Outline platelets.
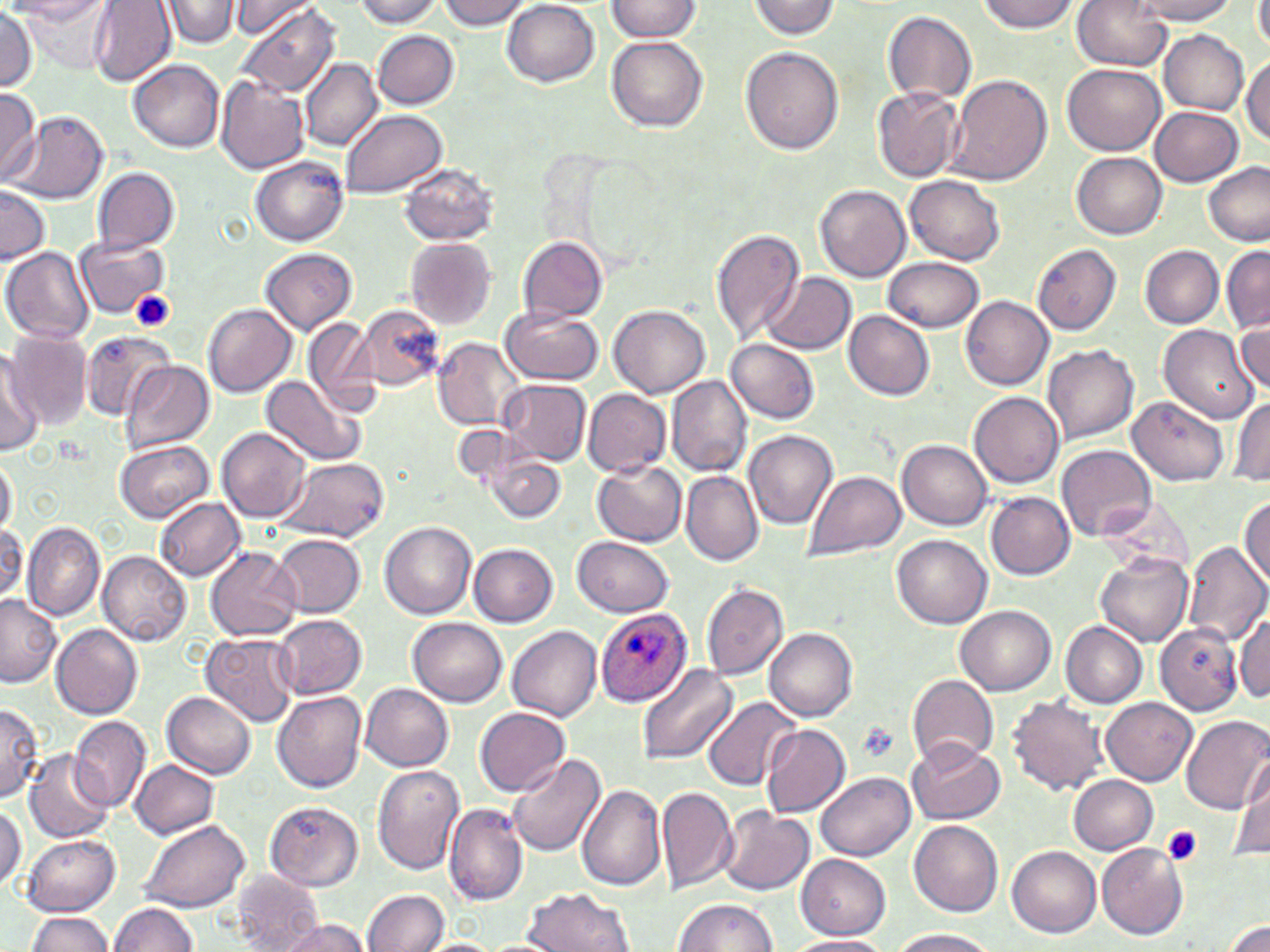

Approximate bounding boxes as (x1,y1)-(x2,y2) corner pairs in pixels.
Platelets: (130,290)-(176,333), (855,721)-(899,762), (1161,826)-(1203,867).

{
  "slide_level_diagnosis": "Plasmodium ovale",
  "modality": "light microscopy",
  "stain": "May-Grünwald-Giemsa",
  "preparation": "thin blood film",
  "image_size": "1270×952 pixels",
  "plasmodium_ovale_infected_red_blood_cell_locations": "approximate bounding boxes as (x1,y1)-(x2,y2) corner pairs in pixels: (597,607)-(692,707)",
  "field_of_view": "single",
  "uninfected_red_blood_cell_locations": "approximate bounding boxes as (x1,y1)-(x2,y2) corner pairs in pixels: (4,0)-(109,23), (21,0)-(120,72), (90,0)-(177,88), (162,0)-(239,47), (353,0)-(444,27), (436,0)-(531,31), (976,0)-(1080,33), (1129,0)-(1240,24), (225,1)-(323,41), (502,1)-(598,86), (604,1)-(703,42), (747,1)-(841,38), (1070,1)-(1174,70), (1252,1)-(1270,51), (238,3)-(342,99), (0,9)-(39,93), (883,11)-(977,104), (1158,29)-(1249,115), (373,30)-(459,110), (608,36)-(708,132), (741,46)-(844,154), (1242,54)-(1270,147), (300,59)-(382,153), (130,60)-(225,152), (1063,64)-(1166,155), (215,75)-(310,173), (947,75)-(1053,187), (872,87)-(964,183), (0,89)-(42,184), (1151,106)-(1243,186), (341,109)-(446,198), (9,111)-(110,204), (1071,152)-(1166,239), (250,155)-(348,247), (1201,160)-(1270,246), (398,163)-(497,247), (92,167)-(179,257), (905,175)-(1006,265), (815,185)-(912,282), (0,186)-(49,266), (710,228)-(804,344), (518,236)-(608,323), (75,237)-(166,318), (404,237)-(497,330), (1033,244)-(1121,336), (1140,245)-(1224,327), (3,247)-(96,343), (1222,247)-(1270,331), (261,248)-(357,334), (884,256)-(983,332), (764,272)-(857,356), (961,296)-(1054,390), (203,303)-(297,397), (357,306)-(444,391), (609,306)-(710,398), (500,308)-(603,385), (844,311)-(935,401), (1233,318)-(1269,397), (304,319)-(380,413), (1157,325)-(1258,424), (79,328)-(175,421), (3,331)-(91,432), (431,337)-(525,432), (726,339)-(819,424), (1042,345)-(1139,445), (0,351)-(41,451), (120,362)-(214,452), (261,375)-(364,466), (667,375)-(751,477), (499,378)-(591,466), (584,388)-(672,478), (968,391)-(1064,487), (1125,396)-(1228,486), (1230,396)-(1270,486), (218,426)-(311,521), (744,429)-(838,530), (898,439)-(993,529), (114,441)-(214,523), (1057,444)-(1157,542), (0,453)-(16,539), (487,453)-(566,523), (277,457)-(387,544), (592,460)-(687,547), (682,471)-(762,565), (804,472)-(905,558), (987,492)-(1074,579), (154,497)-(245,580), (1239,497)-(1270,588), (21,521)-(106,621), (0,522)-(27,607), (379,522)-(477,620), (893,534)-(991,626), (272,535)-(366,617), (573,537)-(674,617), (468,541)-(558,626), (1182,541)-(1269,646), (205,548)-(301,642), (98,550)-(192,646), (1094,552)-(1194,647), (701,582)-(788,681), (0,594)-(64,687), (957,605)-(1057,694), (1234,610)-(1269,703), (275,615)-(367,699), (408,617)-(507,707), (1061,622)-(1147,707), (1154,623)-(1242,714), (51,625)-(144,719), (507,626)-(603,721), (766,628)-(859,721), (203,633)-(299,726), (638,665)-(738,768), (907,673)-(998,770), (361,682)-(453,770), (164,690)-(257,779), (274,691)-(368,792), (1007,694)-(1108,796), (704,696)-(802,792), (1102,696)-(1197,786), (0,703)-(42,802), (475,707)-(570,796), (1180,714)-(1270,814), (69,715)-(150,814), (763,723)-(849,818), (907,738)-(1004,825), (23,749)-(114,844), (509,754)-(606,855), (1242,754)-(1269,831), (131,760)-(217,837), (371,764)-(465,875), (1230,770)-(1270,862), (817,772)-(914,861), (1070,775)-(1158,855), (577,784)-(666,892), (656,784)-(738,894), (265,801)-(363,892), (0,802)-(25,890), (444,802)-(527,904), (719,807)-(815,895), (140,820)-(250,912), (909,820)-(1004,915), (23,835)-(120,916), (1097,843)-(1189,940), (1007,846)-(1101,937), (796,855)-(891,939), (231,871)-(323,951), (523,887)-(637,952), (363,889)-(449,952), (674,898)-(778,952), (110,901)-(198,952), (25,911)-(117,952), (1222,916)-(1270,952), (274,917)-(372,952), (890,928)-(998,952), (785,935)-(894,952), (417,938)-(504,952)",
  "magnification": "1000x"
}